Name the parasite shown.
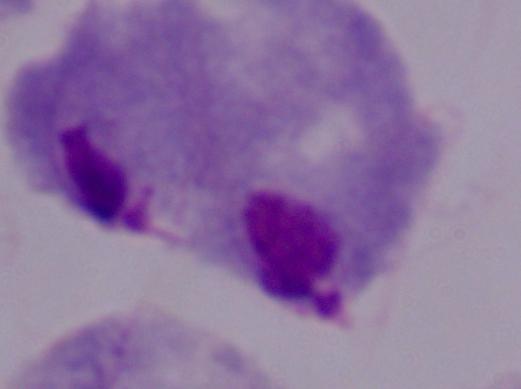
A trichomonad.

Micrograph. 1000x magnification.